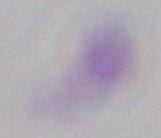

Summary:
  - Magnification: 1000x
  - Modality: photomicrograph
  - Identification: Toxoplasma gondii